Locate every Plasmodium falciparum-infected red blood cell.
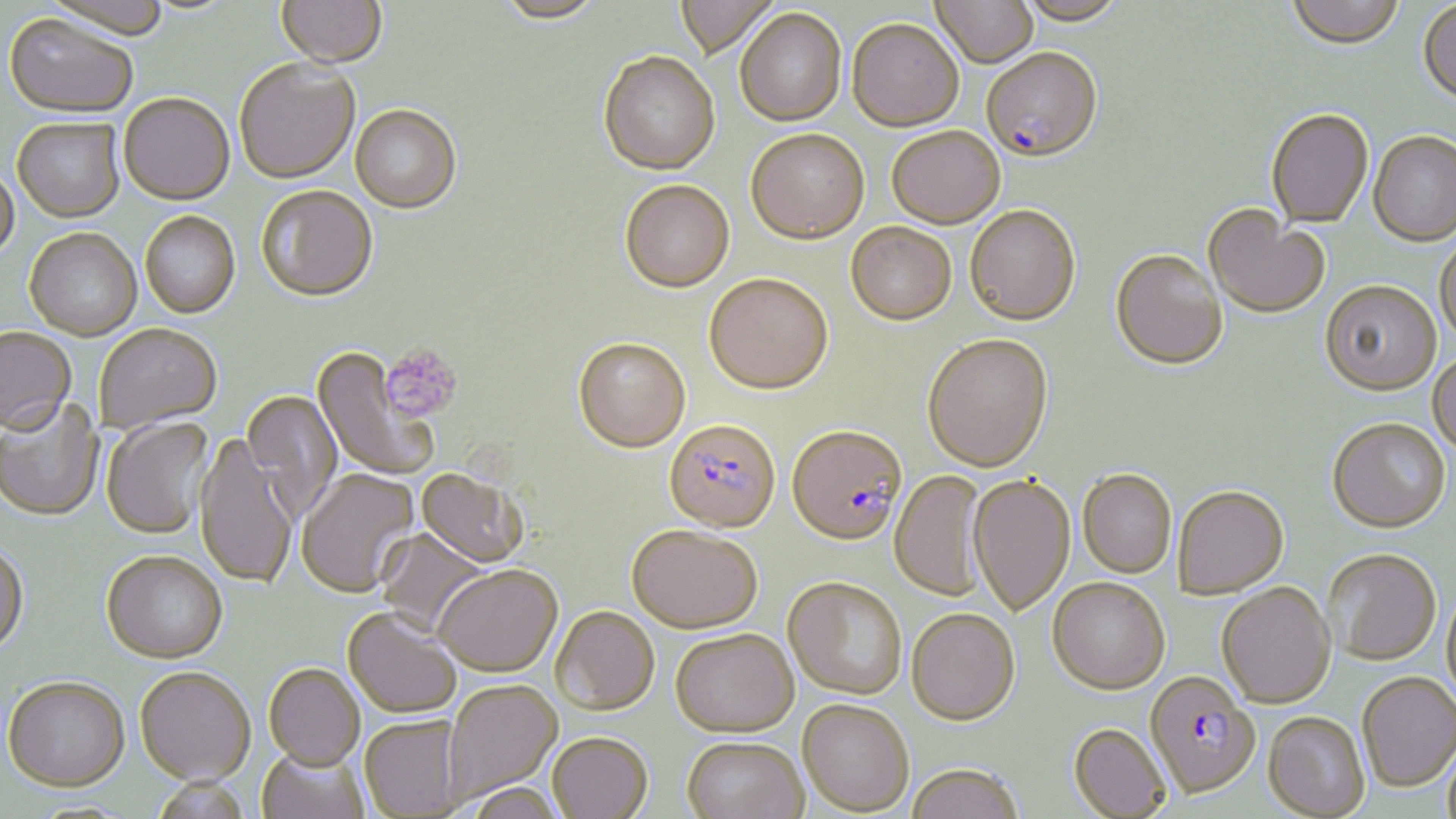

Approximate bounding boxes as (x1, y1, x2, y2) in pixels.
Plasmodium falciparum-infected red blood cells: (981, 47, 1103, 162), (663, 418, 780, 533), (787, 423, 907, 545), (1142, 675, 1262, 802).

Uninfected red blood cell locations: (43, 0, 170, 43), (276, 0, 387, 71), (493, 0, 606, 24), (672, 0, 779, 61), (931, 0, 1038, 67), (1016, 0, 1129, 26), (1286, 0, 1405, 51), (1418, 2, 1456, 107), (735, 7, 847, 127), (2, 16, 137, 121), (847, 19, 964, 132), (598, 52, 720, 176), (234, 61, 361, 186), (118, 96, 235, 208), (350, 106, 462, 215), (1265, 108, 1373, 229), (12, 119, 126, 225), (886, 126, 1005, 228), (746, 128, 869, 244), (1368, 132, 1456, 248), (0, 168, 20, 266), (620, 180, 735, 292), (256, 188, 378, 304), (965, 204, 1081, 324), (1203, 205, 1329, 319), (140, 213, 241, 321), (846, 222, 957, 325), (24, 230, 142, 342), (1435, 235, 1456, 346), (1110, 248, 1228, 369), (704, 273, 833, 394), (1320, 280, 1441, 396), (95, 325, 223, 435), (0, 330, 77, 437), (922, 333, 1053, 471), (573, 336, 691, 453), (311, 348, 438, 482), (1428, 352, 1456, 456), (241, 391, 342, 521), (0, 399, 104, 522), (101, 417, 216, 541), (1327, 417, 1451, 533), (194, 435, 297, 591), (415, 468, 528, 569), (1077, 468, 1177, 578), (297, 470, 420, 600), (889, 470, 988, 602), (968, 473, 1075, 615), (1173, 485, 1289, 597), (627, 524, 762, 634), (376, 528, 491, 635), (0, 546, 29, 659), (1324, 547, 1442, 665), (101, 555, 227, 666), (434, 567, 562, 678), (783, 576, 907, 700), (1048, 576, 1169, 693), (1216, 581, 1336, 708), (1442, 584, 1456, 711), (906, 607, 1020, 724), (551, 608, 660, 718), (342, 609, 462, 721), (669, 630, 799, 739), (263, 667, 365, 773), (135, 670, 255, 790), (1357, 670, 1456, 792), (3, 680, 131, 796), (443, 681, 563, 805), (797, 700, 914, 816), (1263, 711, 1369, 818), (359, 718, 463, 817), (1068, 722, 1171, 818), (1443, 734, 1456, 819), (548, 736, 653, 819), (681, 739, 809, 819), (257, 750, 370, 819), (906, 763, 1024, 819), (151, 780, 250, 819), (464, 784, 568, 819). Platelet locations: (380, 345, 462, 423). Slide-level diagnosis: Plasmodium falciparum. May-Grünwald-Giemsa stain. Captured at 1000x magnification. Light microscopy. Image is 1456×819 pixels. Thin blood film. Single field of view.